Locate every blood parasite and identify its species.
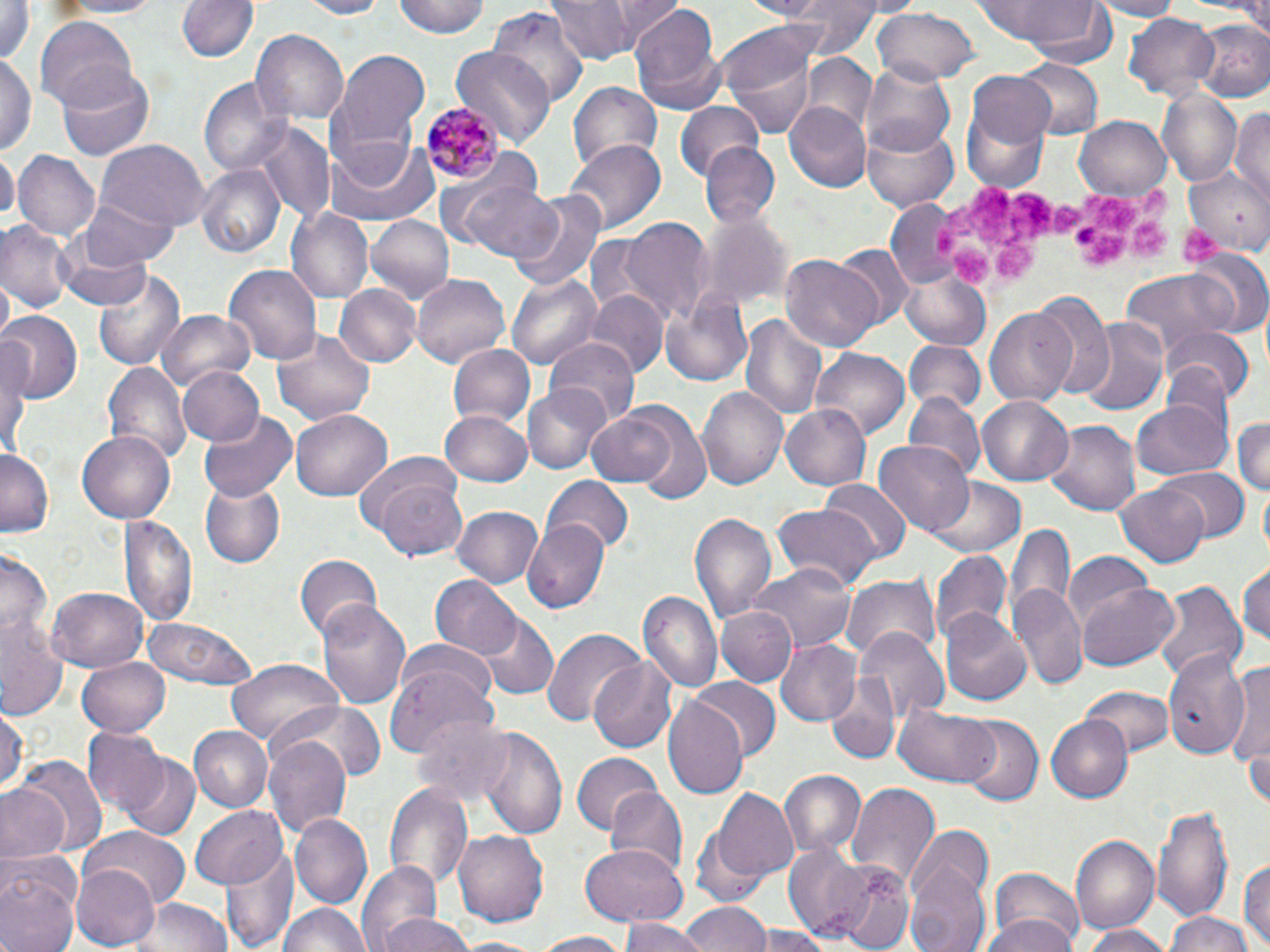
Approximate bounding boxes as (x1, y1, x2, y2) in pixels.
Plasmodium malariae-infected red blood cells: (423, 103, 501, 185).
No Plasmodium falciparum, Plasmodium ovale, Plasmodium vivax, Babesia divergens, or Trypanosoma brucei observed.

Summary:
  - Uninfected red blood cell locations: (1, 0, 36, 75), (52, 0, 164, 20), (175, 0, 257, 65), (293, 0, 392, 18), (394, 0, 491, 39), (551, 0, 636, 64), (606, 0, 687, 50), (733, 0, 835, 20), (776, 0, 888, 55), (970, 0, 1112, 49), (1085, 0, 1184, 20), (628, 2, 724, 109), (487, 6, 590, 110), (870, 9, 981, 86), (1124, 13, 1221, 98), (37, 14, 138, 111), (1189, 18, 1270, 103), (251, 30, 346, 123), (718, 36, 819, 142), (451, 47, 553, 147), (337, 52, 430, 145), (0, 53, 35, 156), (801, 55, 874, 132), (1013, 58, 1102, 140), (863, 62, 955, 155), (58, 67, 154, 159), (965, 69, 1056, 158), (199, 77, 288, 175), (568, 81, 663, 174), (1157, 90, 1242, 187), (674, 101, 765, 178), (785, 103, 870, 192), (960, 105, 1052, 195), (1233, 105, 1269, 202), (1074, 115, 1171, 200), (861, 121, 959, 210), (253, 125, 335, 223), (322, 136, 438, 229), (565, 140, 664, 234), (95, 141, 208, 233), (699, 142, 781, 230), (1, 149, 17, 224), (12, 150, 100, 243), (197, 164, 283, 259), (1187, 165, 1270, 252), (459, 181, 563, 262), (508, 189, 609, 295), (80, 195, 180, 267), (884, 197, 965, 290), (289, 208, 372, 300), (365, 215, 453, 305), (616, 216, 714, 325), (698, 216, 788, 313), (1, 221, 73, 313), (57, 240, 153, 310), (829, 243, 911, 328), (1187, 252, 1270, 338), (781, 255, 884, 351), (224, 265, 322, 366), (93, 267, 185, 373), (1119, 267, 1243, 355), (508, 270, 603, 368), (903, 270, 987, 344), (413, 273, 512, 367), (334, 283, 419, 369), (661, 287, 753, 387), (584, 292, 668, 379), (1031, 294, 1114, 399), (985, 308, 1079, 408), (160, 309, 255, 391), (0, 312, 82, 403), (741, 314, 826, 422), (1077, 318, 1168, 417), (1160, 325, 1255, 404), (272, 326, 375, 426), (544, 338, 640, 430), (902, 341, 986, 415), (448, 344, 534, 429), (0, 349, 28, 461), (813, 349, 910, 438), (103, 362, 188, 463), (174, 366, 264, 448), (697, 385, 787, 494), (523, 387, 609, 473), (903, 394, 985, 485), (977, 396, 1072, 483), (1130, 398, 1232, 482), (781, 403, 873, 490), (585, 405, 690, 492), (291, 409, 391, 500), (627, 409, 713, 506), (201, 411, 297, 501), (439, 411, 533, 486), (1231, 413, 1270, 500), (1047, 418, 1140, 517), (75, 432, 176, 525), (876, 439, 974, 538), (0, 446, 54, 533), (1155, 467, 1248, 543), (371, 476, 468, 561), (540, 478, 635, 554), (820, 480, 911, 562), (927, 480, 1027, 560), (201, 481, 286, 567), (1114, 485, 1209, 565), (772, 503, 881, 594), (454, 506, 545, 590), (123, 512, 198, 628), (690, 512, 777, 627), (1005, 516, 1074, 633), (520, 520, 610, 614), (930, 546, 1012, 647), (0, 552, 50, 641), (293, 554, 382, 642), (1062, 554, 1155, 634), (1238, 559, 1269, 652), (750, 564, 856, 653), (839, 572, 942, 663), (431, 574, 521, 661), (1153, 579, 1246, 686), (1077, 580, 1180, 671), (1012, 582, 1087, 690), (46, 587, 147, 673), (640, 591, 722, 694), (317, 598, 412, 708), (716, 607, 795, 684), (941, 611, 1031, 706), (475, 612, 558, 698), (0, 614, 66, 720), (142, 615, 261, 692), (542, 626, 647, 726), (856, 628, 948, 721), (774, 638, 861, 727), (401, 639, 499, 715), (1161, 649, 1250, 760), (76, 656, 169, 737), (590, 657, 679, 751), (228, 659, 343, 749), (1224, 659, 1270, 781), (386, 662, 495, 759), (689, 678, 779, 764), (825, 680, 899, 764), (1082, 686, 1173, 760), (663, 697, 747, 800), (268, 702, 383, 787), (895, 703, 998, 788), (0, 705, 26, 792), (1044, 713, 1132, 802), (413, 714, 515, 805), (960, 717, 1044, 807), (188, 726, 273, 813), (477, 726, 568, 838), (82, 729, 166, 815), (265, 734, 353, 841), (122, 752, 199, 838), (571, 752, 658, 836), (16, 757, 106, 858), (778, 770, 863, 858), (1, 779, 73, 864), (847, 779, 941, 889), (385, 782, 471, 889), (605, 786, 688, 878), (708, 788, 803, 888), (191, 803, 291, 890), (1154, 805, 1232, 926), (291, 813, 372, 908), (78, 829, 189, 911), (454, 829, 548, 925), (1071, 835, 1159, 934), (905, 841, 993, 952), (223, 842, 298, 952), (577, 844, 688, 926), (784, 844, 869, 938), (1239, 857, 1269, 948), (357, 862, 445, 952), (836, 863, 914, 950), (71, 864, 161, 950), (0, 869, 78, 952), (988, 871, 1087, 952), (128, 895, 234, 952), (1197, 898, 1270, 952), (678, 900, 767, 952), (277, 901, 372, 952), (1163, 913, 1258, 952), (376, 914, 477, 952), (979, 915, 1080, 952), (622, 917, 703, 952), (1078, 924, 1172, 952), (751, 926, 831, 952), (529, 931, 637, 952), (449, 936, 552, 952)
  - Platelet locations: (967, 181, 1011, 249), (1133, 183, 1177, 217), (1003, 190, 1058, 246), (1088, 191, 1140, 230), (1047, 201, 1079, 234), (1124, 216, 1170, 259), (1177, 223, 1227, 266), (1075, 224, 1131, 266), (928, 225, 965, 260), (995, 238, 1038, 287), (950, 246, 994, 284)
  - Slide-level diagnosis: Plasmodium malariae
  - Stain: May-Grünwald-Giemsa
  - Magnification: 1000x
  - Field of view: one of a larger specimen
  - Preparation: thin blood film
  - Image size: 1270×952 pixels
  - Modality: light microscopy